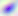

Summary:
  - Magnification: 400x
  - Modality: photomicrograph
  - Identification: Toxoplasma gondii